Assess the morphology of the erythrocytes.
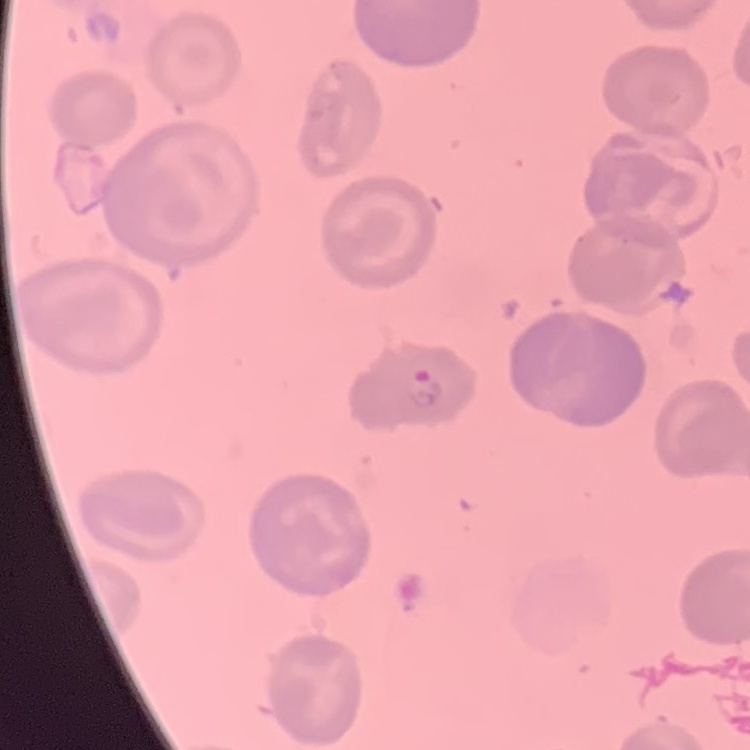
No rouleaux formation.

Stained with either Field's or Giemsa. Square crop of a larger photomicrograph. Thin blood film.